Assess this cell for malaria.
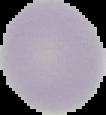
It is uninfected.

Segmented cell region on a black background. From a thin blood film. Image is 106×115 pixels.